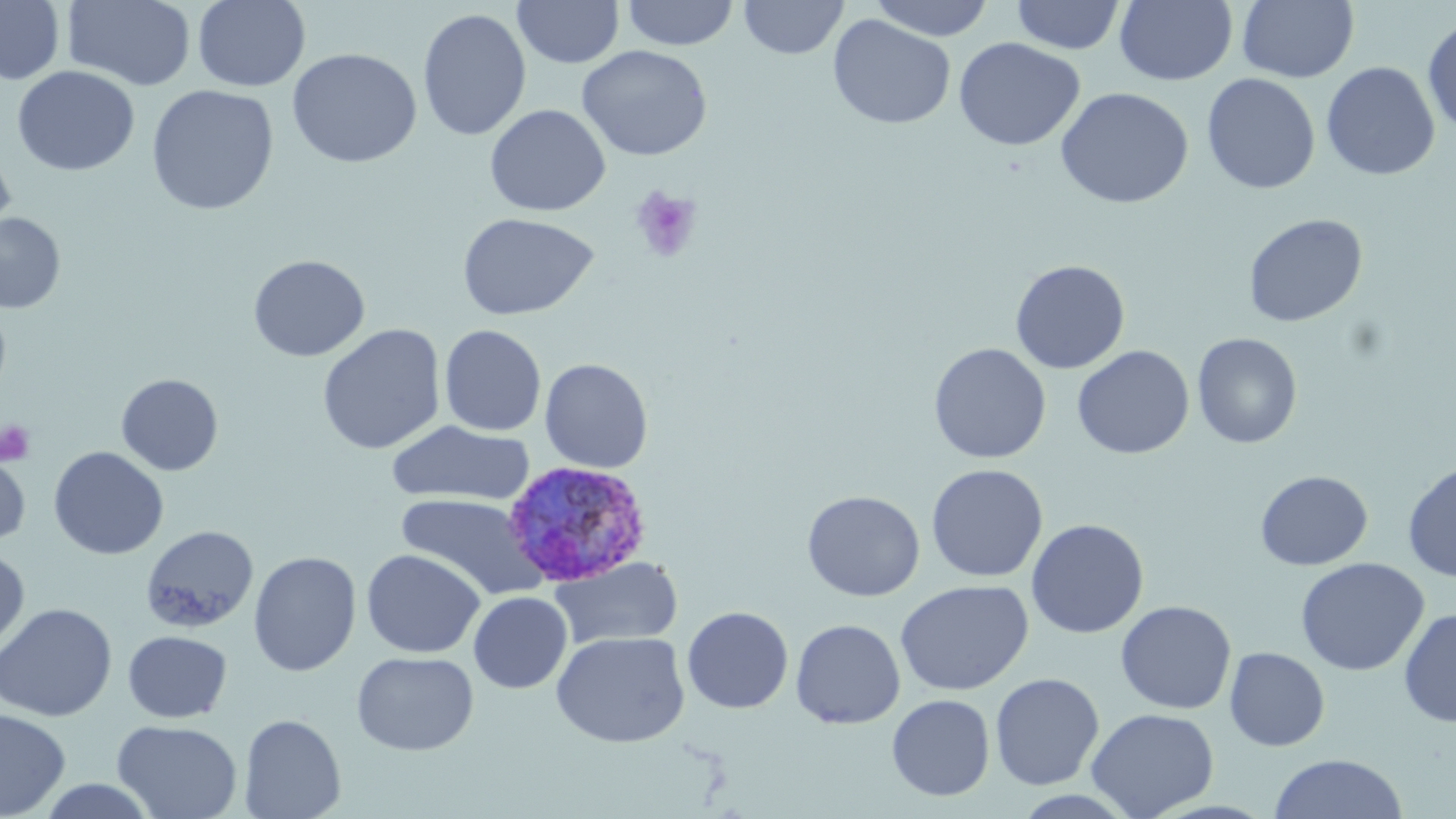 Approximate bounding boxes as named x1/y1/x2/y2 corners in pixels. Platelet locations: (x1=628, y1=184, x2=703, y2=263), (x1=0, y1=419, x2=36, y2=465). Plasmodium ovale-infected red blood cell locations: (x1=501, y1=459, x2=653, y2=588). Uninfected red blood cell locations: (x1=0, y1=0, x2=65, y2=85), (x1=63, y1=0, x2=196, y2=91), (x1=192, y1=0, x2=310, y2=92), (x1=621, y1=0, x2=740, y2=50), (x1=739, y1=0, x2=847, y2=60), (x1=867, y1=0, x2=997, y2=41), (x1=1010, y1=0, x2=1126, y2=55), (x1=512, y1=1, x2=624, y2=69), (x1=1010, y1=1, x2=1237, y2=63), (x1=1114, y1=1, x2=1238, y2=86), (x1=1237, y1=1, x2=1359, y2=84), (x1=417, y1=8, x2=532, y2=142), (x1=828, y1=14, x2=956, y2=129), (x1=1422, y1=15, x2=1456, y2=136), (x1=954, y1=37, x2=1085, y2=151), (x1=577, y1=45, x2=712, y2=161), (x1=287, y1=48, x2=422, y2=169), (x1=1321, y1=61, x2=1440, y2=181), (x1=12, y1=65, x2=139, y2=176), (x1=1201, y1=73, x2=1320, y2=195), (x1=146, y1=85, x2=279, y2=216), (x1=1055, y1=87, x2=1194, y2=209), (x1=485, y1=104, x2=610, y2=216), (x1=0, y1=146, x2=16, y2=249), (x1=0, y1=213, x2=65, y2=314), (x1=457, y1=213, x2=599, y2=321), (x1=1243, y1=213, x2=1368, y2=327), (x1=247, y1=254, x2=370, y2=362), (x1=1010, y1=259, x2=1130, y2=374), (x1=316, y1=324, x2=446, y2=455), (x1=439, y1=324, x2=547, y2=436), (x1=1192, y1=332, x2=1303, y2=449), (x1=928, y1=342, x2=1051, y2=464), (x1=1072, y1=345, x2=1195, y2=460), (x1=539, y1=358, x2=653, y2=473), (x1=116, y1=373, x2=223, y2=475), (x1=386, y1=420, x2=536, y2=507), (x1=48, y1=447, x2=169, y2=560), (x1=0, y1=448, x2=32, y2=550), (x1=1402, y1=460, x2=1456, y2=582), (x1=926, y1=464, x2=1048, y2=582), (x1=1255, y1=470, x2=1373, y2=571), (x1=801, y1=490, x2=925, y2=601), (x1=396, y1=493, x2=543, y2=600), (x1=1026, y1=518, x2=1149, y2=639), (x1=141, y1=525, x2=259, y2=633), (x1=0, y1=547, x2=29, y2=652), (x1=361, y1=549, x2=485, y2=658), (x1=248, y1=551, x2=361, y2=676), (x1=550, y1=556, x2=683, y2=651), (x1=1295, y1=557, x2=1430, y2=676), (x1=895, y1=580, x2=1033, y2=696), (x1=468, y1=591, x2=572, y2=694), (x1=1116, y1=600, x2=1236, y2=715), (x1=0, y1=603, x2=117, y2=722), (x1=682, y1=606, x2=794, y2=714), (x1=1398, y1=608, x2=1456, y2=727), (x1=790, y1=619, x2=906, y2=729), (x1=123, y1=630, x2=232, y2=723), (x1=551, y1=631, x2=690, y2=748), (x1=1225, y1=647, x2=1330, y2=751), (x1=352, y1=651, x2=479, y2=755), (x1=990, y1=672, x2=1104, y2=790), (x1=887, y1=694, x2=995, y2=801), (x1=1087, y1=707, x2=1220, y2=818), (x1=0, y1=709, x2=70, y2=818), (x1=239, y1=713, x2=346, y2=819), (x1=111, y1=718, x2=243, y2=819), (x1=1269, y1=753, x2=1409, y2=818), (x1=35, y1=778, x2=161, y2=818). Slide-level diagnosis: Plasmodium ovale. One field of a larger specimen. May-Grünwald-Giemsa stain. Thin blood smear. Optical microscopy. Image is 1456×819 pixels. Captured at 1000x magnification.